Give the position of every leukocyte visible.
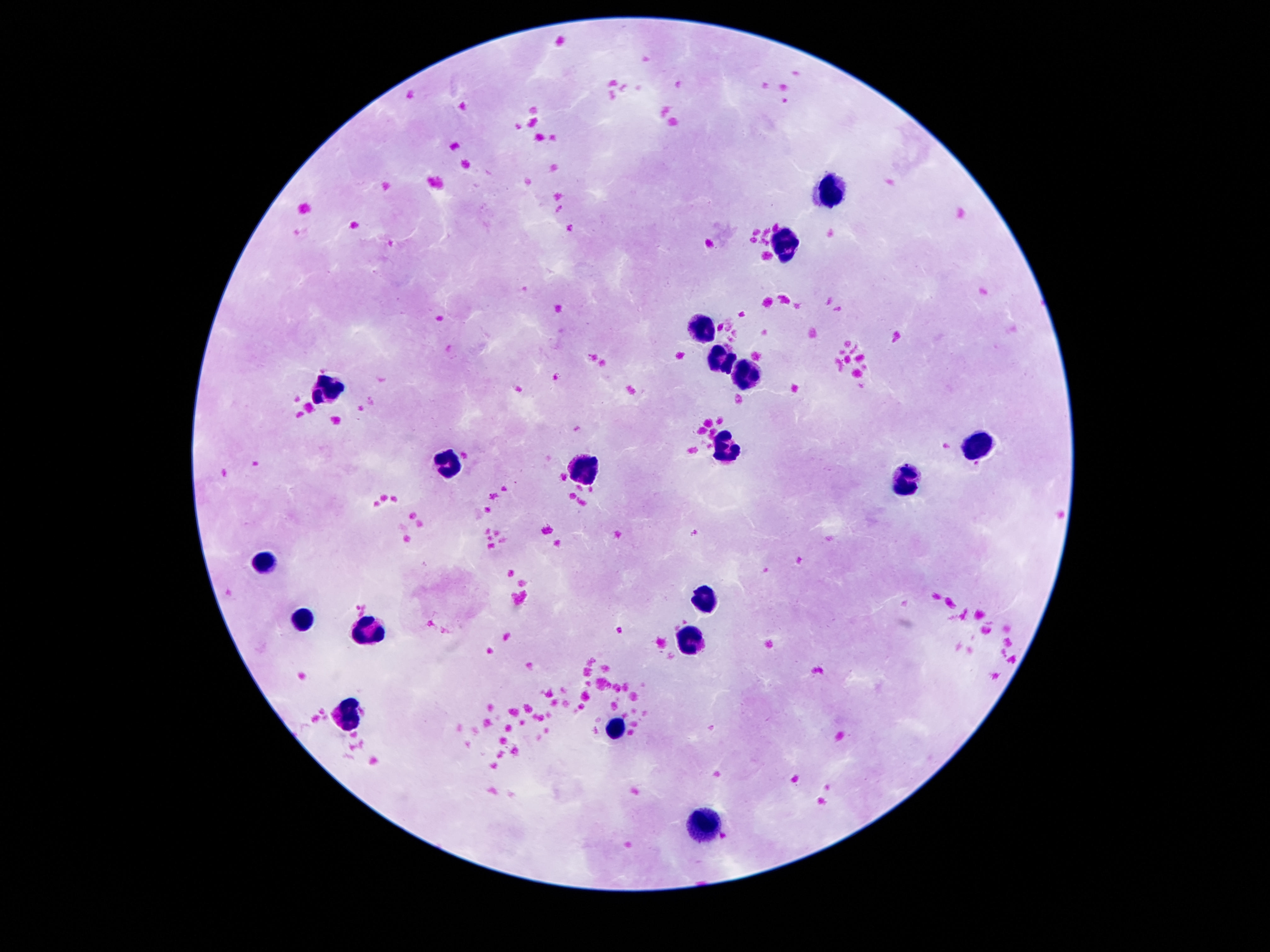

Approximate centers as {x, y} in pixels.
Leukocytes: {831, 191}, {790, 243}, {704, 326}, {721, 358}, {740, 370}, {329, 383}, {980, 442}, {733, 448}, {450, 467}, {588, 473}, {908, 481}, {267, 558}, {708, 597}, {301, 619}, {366, 631}, {691, 638}, {348, 715}, {619, 726}, {708, 825}.

stain = Giemsa
patient malaria status = negative
magnification = 100x
capture = smartphone camera through the microscope eyepiece
image size = 1270×952 pixels
field of view = single
preparation = thick peripheral-blood smear